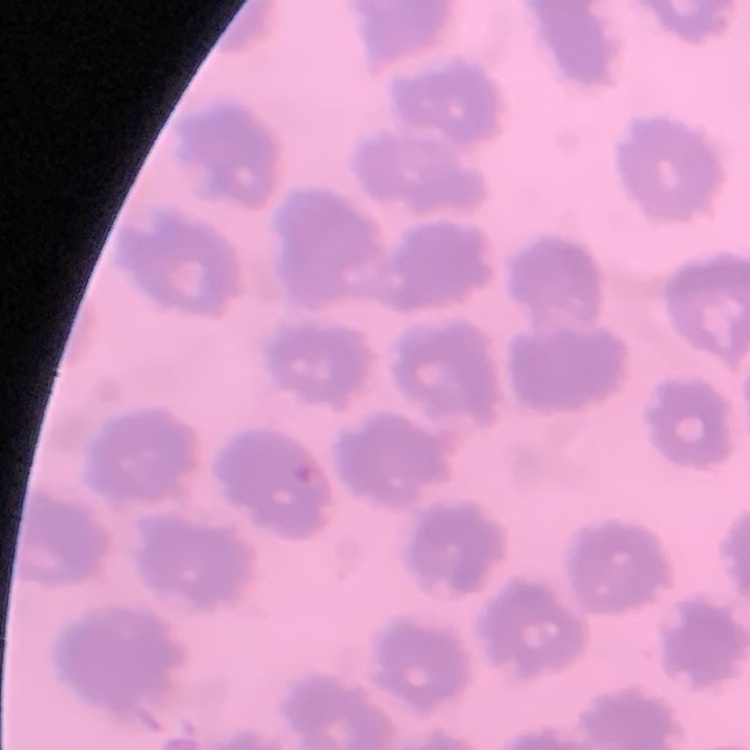

Summary:
  - Red blood cell morphology: no rouleaux formation
  - Stain: Field's or Giemsa
  - Image type: square crop of a larger photomicrograph
  - Preparation: thin blood smear